Outline each uninfected red blood cell.
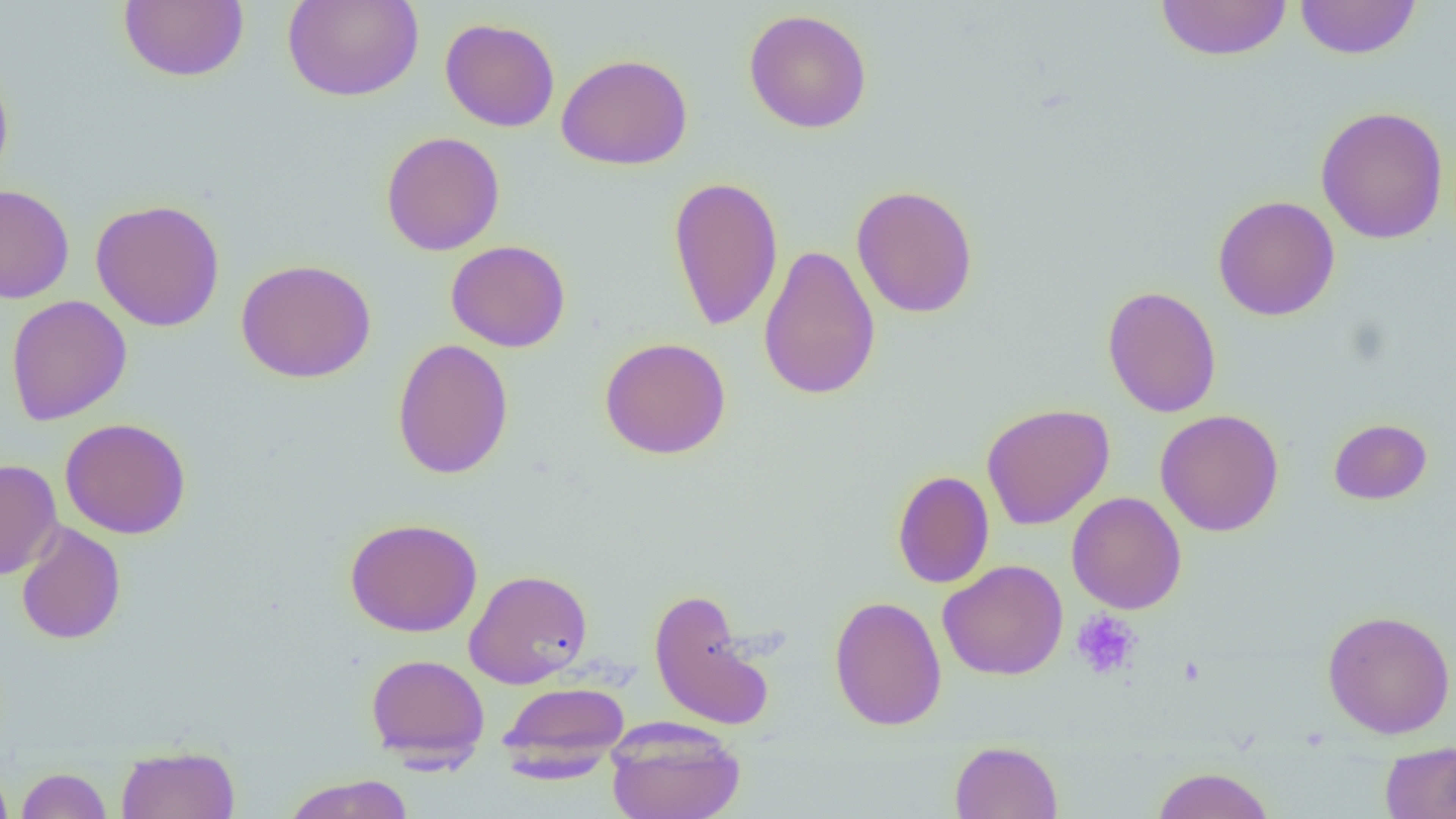

Approximate bounding boxes as named x1/y1/x2/y2 corners in pixels.
Uninfected red blood cells: (x1=118, y1=0, x2=249, y2=83), (x1=282, y1=0, x2=424, y2=102), (x1=1294, y1=0, x2=1422, y2=60), (x1=1155, y1=1, x2=1292, y2=62), (x1=743, y1=9, x2=873, y2=134), (x1=440, y1=17, x2=560, y2=132), (x1=556, y1=52, x2=693, y2=171), (x1=0, y1=62, x2=14, y2=186), (x1=1315, y1=105, x2=1450, y2=245), (x1=380, y1=131, x2=505, y2=256), (x1=667, y1=175, x2=784, y2=331), (x1=0, y1=184, x2=75, y2=303), (x1=851, y1=184, x2=979, y2=319), (x1=1212, y1=195, x2=1340, y2=321), (x1=90, y1=198, x2=225, y2=332), (x1=446, y1=240, x2=570, y2=352), (x1=757, y1=243, x2=881, y2=402), (x1=236, y1=258, x2=376, y2=383), (x1=1102, y1=286, x2=1222, y2=418), (x1=5, y1=295, x2=132, y2=425), (x1=599, y1=337, x2=732, y2=460), (x1=392, y1=338, x2=513, y2=479), (x1=981, y1=403, x2=1115, y2=530), (x1=1155, y1=409, x2=1284, y2=537), (x1=60, y1=418, x2=191, y2=539), (x1=1328, y1=418, x2=1432, y2=505), (x1=0, y1=459, x2=63, y2=580), (x1=893, y1=470, x2=994, y2=588), (x1=1066, y1=492, x2=1187, y2=614), (x1=344, y1=517, x2=483, y2=637), (x1=15, y1=521, x2=126, y2=645), (x1=938, y1=559, x2=1068, y2=680), (x1=464, y1=568, x2=594, y2=688), (x1=648, y1=587, x2=774, y2=731), (x1=829, y1=595, x2=947, y2=731), (x1=1321, y1=609, x2=1456, y2=739), (x1=365, y1=653, x2=490, y2=767), (x1=498, y1=681, x2=630, y2=777), (x1=606, y1=721, x2=745, y2=819), (x1=1380, y1=740, x2=1456, y2=819), (x1=949, y1=741, x2=1063, y2=819), (x1=115, y1=745, x2=240, y2=819), (x1=0, y1=766, x2=14, y2=818), (x1=1151, y1=766, x2=1276, y2=819), (x1=16, y1=767, x2=112, y2=819), (x1=283, y1=773, x2=415, y2=819).

Platelet locations: (x1=1071, y1=610, x2=1142, y2=680). Slide-level diagnosis: negative for blood parasites. Captured at 1000x magnification. Image is 1456×819 pixels. Optical microscopy. Thin blood film. Single field of view.